Report the malaria status of this cell.
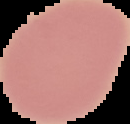
It is uninfected.

preparation = thin blood smear
image size = 130×124 pixels
image type = segmented cell region on a black background